Report the malaria status of this cell.
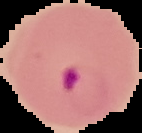

Parasitized.

Image is 142×133 pixels. From a thin blood film. Segmented cell region on a black background.